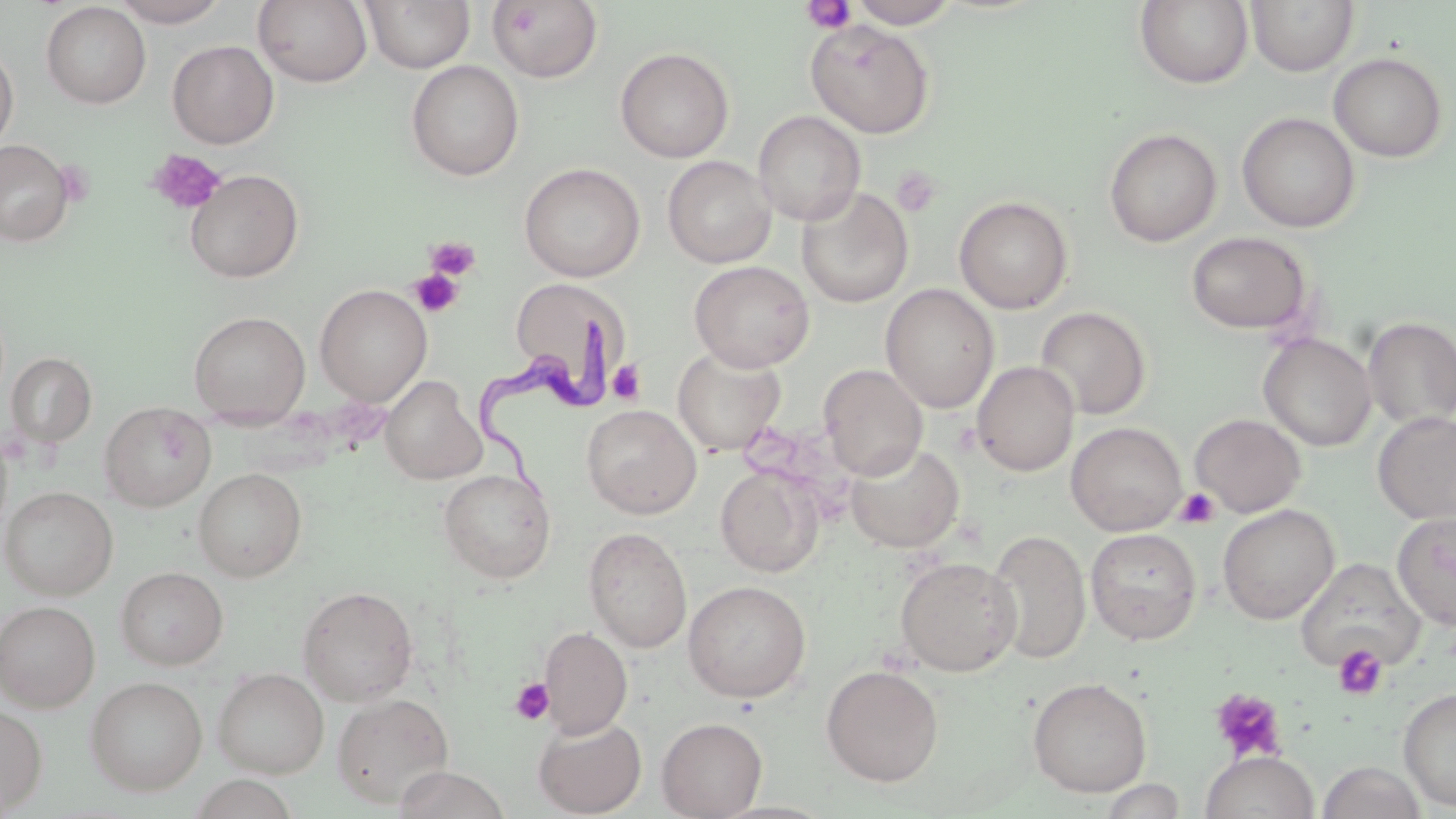

Summary:
  - Coordinate format: approximate bounding boxes as (x1, y1, x2, y2) in pixels
  - Trypanosoma brucei locations: (476, 310, 610, 506)
  - Platelet locations: (801, 1, 856, 33), (147, 148, 226, 214), (892, 165, 941, 218), (425, 237, 481, 280), (409, 269, 464, 317), (607, 359, 645, 405), (1175, 487, 1220, 529), (1333, 644, 1388, 700), (510, 677, 553, 725), (1210, 687, 1287, 762)
  - Uninfected red blood cell locations: (110, 0, 230, 27), (253, 0, 373, 87), (361, 0, 475, 73), (849, 0, 959, 28), (1246, 0, 1359, 76), (487, 1, 604, 84), (1134, 1, 1255, 89), (40, 2, 151, 109), (805, 19, 935, 139), (167, 40, 279, 148), (0, 44, 19, 151), (615, 47, 734, 163), (1329, 53, 1448, 162), (406, 60, 524, 180), (753, 110, 866, 226), (1237, 112, 1360, 232), (1103, 127, 1222, 247), (0, 139, 74, 246), (662, 156, 777, 268), (519, 162, 645, 282), (185, 169, 304, 283), (796, 187, 914, 308), (954, 195, 1073, 314), (1186, 231, 1312, 334), (689, 260, 815, 372), (510, 276, 630, 408), (315, 284, 432, 406), (881, 284, 999, 414), (1035, 306, 1152, 420), (188, 310, 311, 426), (1363, 317, 1456, 429), (1259, 333, 1376, 451), (672, 346, 786, 455), (5, 351, 97, 448), (972, 361, 1079, 477), (819, 364, 927, 480), (380, 375, 486, 484), (100, 401, 216, 512), (581, 403, 702, 518), (1372, 412, 1456, 524), (1189, 413, 1306, 517), (1066, 421, 1187, 536), (845, 442, 964, 553), (716, 465, 824, 577), (194, 467, 307, 581), (438, 468, 556, 583), (0, 485, 118, 600), (1217, 504, 1339, 624), (1392, 511, 1456, 630), (584, 527, 692, 652), (1085, 527, 1202, 645), (987, 529, 1091, 664), (895, 556, 1021, 677), (1295, 558, 1424, 672), (115, 566, 228, 670), (682, 580, 811, 702), (297, 585, 419, 705), (0, 600, 100, 712), (540, 625, 632, 738), (821, 664, 944, 787), (212, 668, 329, 778), (85, 676, 207, 795), (1027, 677, 1152, 797), (1398, 687, 1456, 812), (331, 693, 454, 808), (0, 703, 48, 814), (534, 716, 647, 817), (656, 717, 768, 818), (1200, 750, 1319, 819), (1317, 761, 1426, 819), (391, 766, 512, 819), (187, 773, 299, 818)
  - Slide-level diagnosis: Trypanosoma brucei
  - Preparation: thin blood film
  - Image size: 1456×819 pixels
  - Stain: May-Grünwald-Giemsa
  - Magnification: 1000x
  - Field of view: one of a larger specimen
  - Modality: optical microscopy